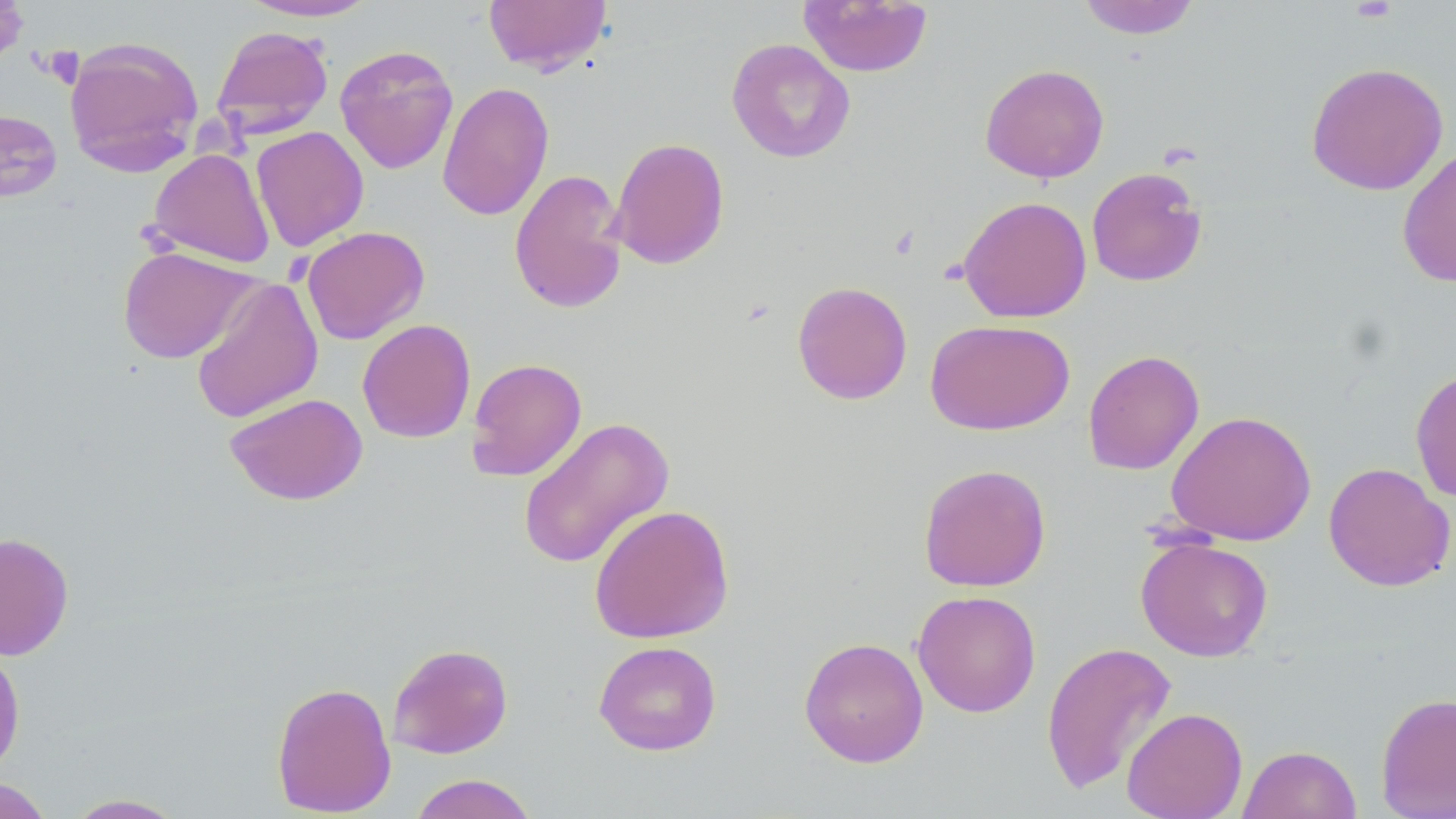 Approximate bounding boxes as (x1, y1, x2, y2) in pixels. Uninfected red blood cell locations: (483, 0, 612, 75), (798, 0, 934, 77), (1078, 0, 1201, 39), (238, 1, 381, 22), (211, 25, 334, 138), (63, 36, 204, 176), (727, 37, 855, 163), (334, 44, 459, 174), (1306, 61, 1449, 196), (980, 63, 1109, 183), (437, 81, 555, 221), (1, 108, 63, 202), (251, 126, 370, 252), (609, 136, 730, 270), (1397, 145, 1456, 288), (149, 148, 275, 269), (1086, 167, 1208, 287), (509, 168, 629, 315), (957, 195, 1092, 323), (301, 225, 429, 344), (117, 245, 258, 364), (190, 275, 324, 425), (792, 281, 912, 405), (356, 318, 476, 443), (925, 319, 1075, 436), (1082, 349, 1204, 475), (466, 357, 587, 481), (1411, 368, 1456, 503), (225, 392, 368, 505), (1165, 410, 1316, 546), (516, 417, 674, 570), (1323, 462, 1455, 592), (917, 463, 1052, 592), (588, 504, 735, 644), (0, 532, 74, 660), (1135, 535, 1274, 661), (912, 590, 1041, 717), (798, 636, 929, 768), (593, 640, 722, 756), (1040, 640, 1178, 796), (0, 642, 25, 776), (387, 642, 513, 759), (271, 680, 397, 817), (1375, 693, 1456, 818), (1122, 707, 1248, 819), (1238, 745, 1361, 819), (407, 774, 539, 819), (0, 778, 54, 819), (63, 794, 188, 818). Slide-level diagnosis: negative for blood parasites. Captured at 1000x magnification. One field of a larger specimen. May-Grünwald-Giemsa stain. Thin blood film. Optical microscopy. Image is 1456×819 pixels.